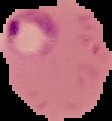
image type = segmented cell region on a black background
preparation = thin blood smear
result = malaria parasites identified
image size = 112×121 pixels